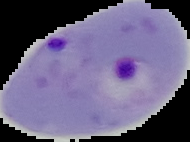

result: malaria parasites identified
image_size: 190×142 pixels
image_type: segmented cell region with the area outside set to black
preparation: thin blood smear